Comment on the morphology of the erythrocytes.
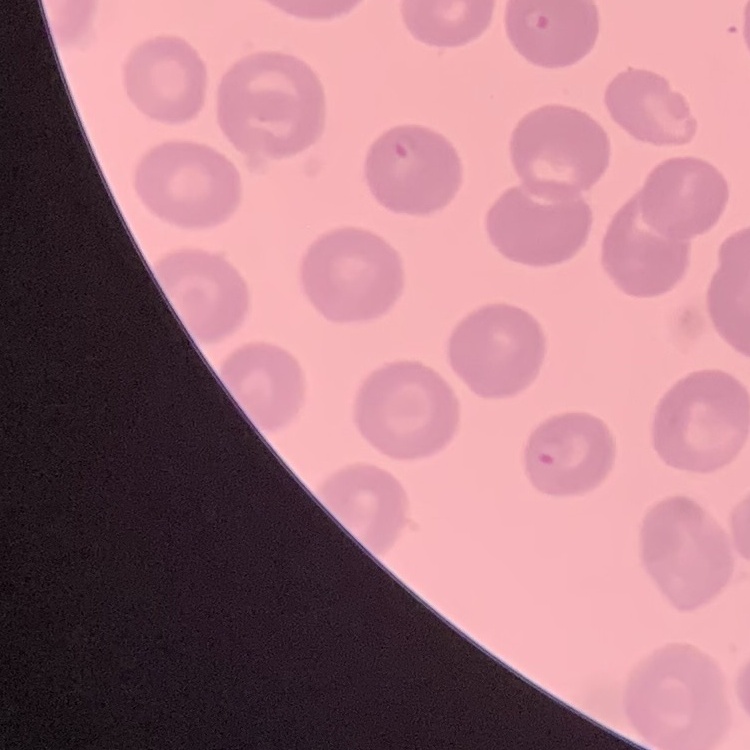

No rouleaux formation.

{
  "image_type": "one tile cut from a larger photomicrograph",
  "preparation": "thin blood film",
  "stain": "Field's or Giemsa"
}